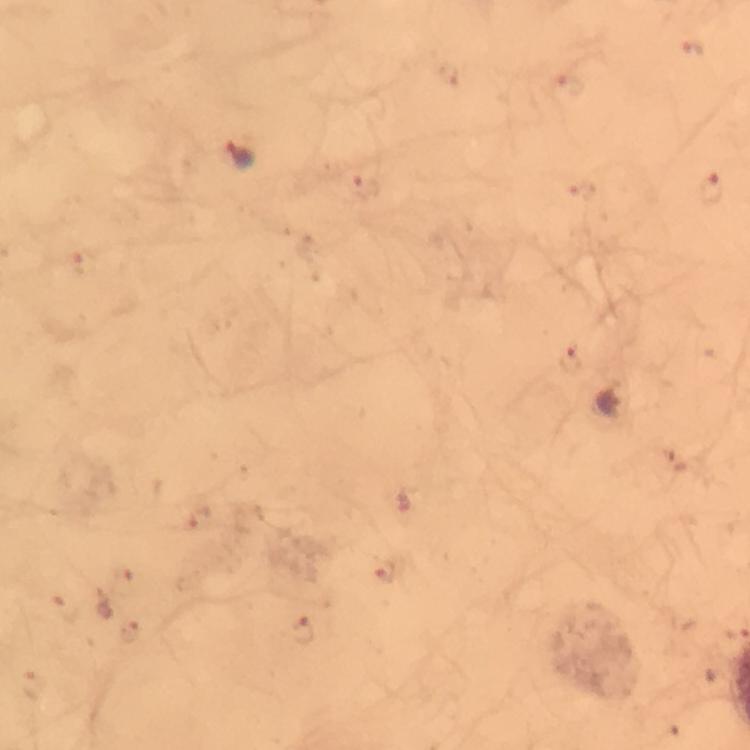
Approximate object centers, in pixels from the top-left corner. Malaria parasite locations: (x=693, y=49), (x=450, y=76), (x=571, y=85), (x=241, y=156), (x=366, y=187), (x=711, y=189), (x=584, y=191), (x=85, y=265), (x=571, y=362), (x=679, y=462), (x=201, y=520), (x=386, y=573), (x=123, y=582), (x=66, y=607), (x=302, y=629), (x=130, y=633). From a diagnostic examination for malaria. Photographed through the microscope with a smartphone camera. Thick blood smear. Cropped region of a single field of view. Immersion oil was used. 100x magnification. Image is 750×750 pixels. Giemsa-stained preparation.